Assess this cell for malaria.
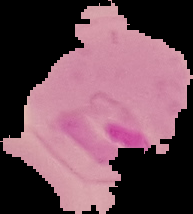
It is parasitized.

Summary:
  - Preparation: thin blood smear
  - Image size: 193×214 pixels
  - Image type: segmented cell region on a black background